Identify the parasite.
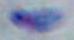

Toxoplasma gondii.

{
  "magnification": "1000x",
  "modality": "micrograph"
}